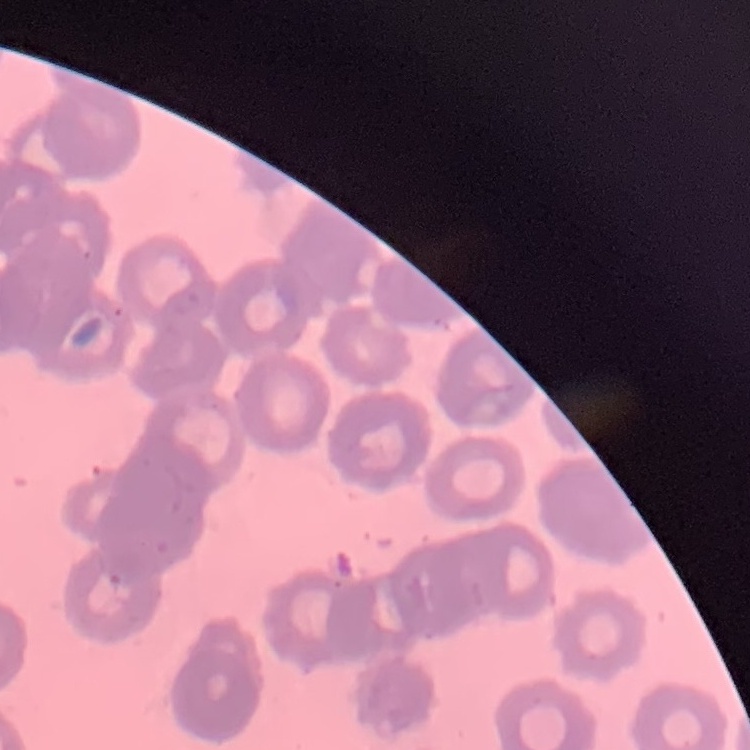

The erythrocytes show rouleaux formation. Thin blood film. One tile cut from a larger photomicrograph. Stained with either Field's or Giemsa.